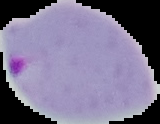
The area outside the segmented cell region is set to black. Image is 160×124 pixels. Malaria status: parasitized. From a thin blood smear.